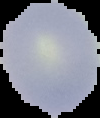

preparation: thin blood film
result: no malaria parasites detected
image_size: 100×118 pixels
image_type: segmented cell region with the area outside set to black